State which parasite is depicted.
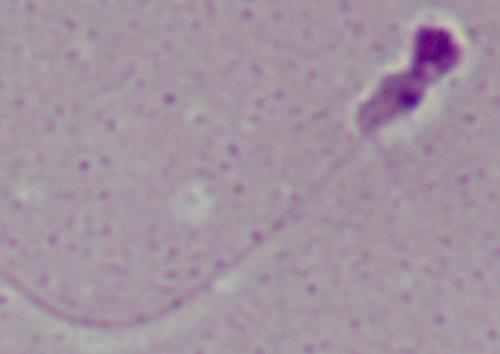
This is Leishmania.

Summary:
  - Modality: micrograph
  - Magnification: 1000x